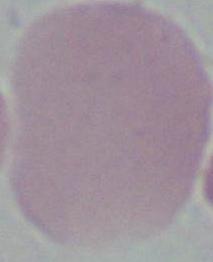
Summary:
  - Identification: red blood cell
  - Magnification: 1000x
  - Modality: micrograph